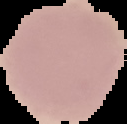
image_size: 127×124 pixels
malaria_status: uninfected
preparation: thin blood smear
image_type: segmented cell region on a black background